Locate and identify every blood parasite.
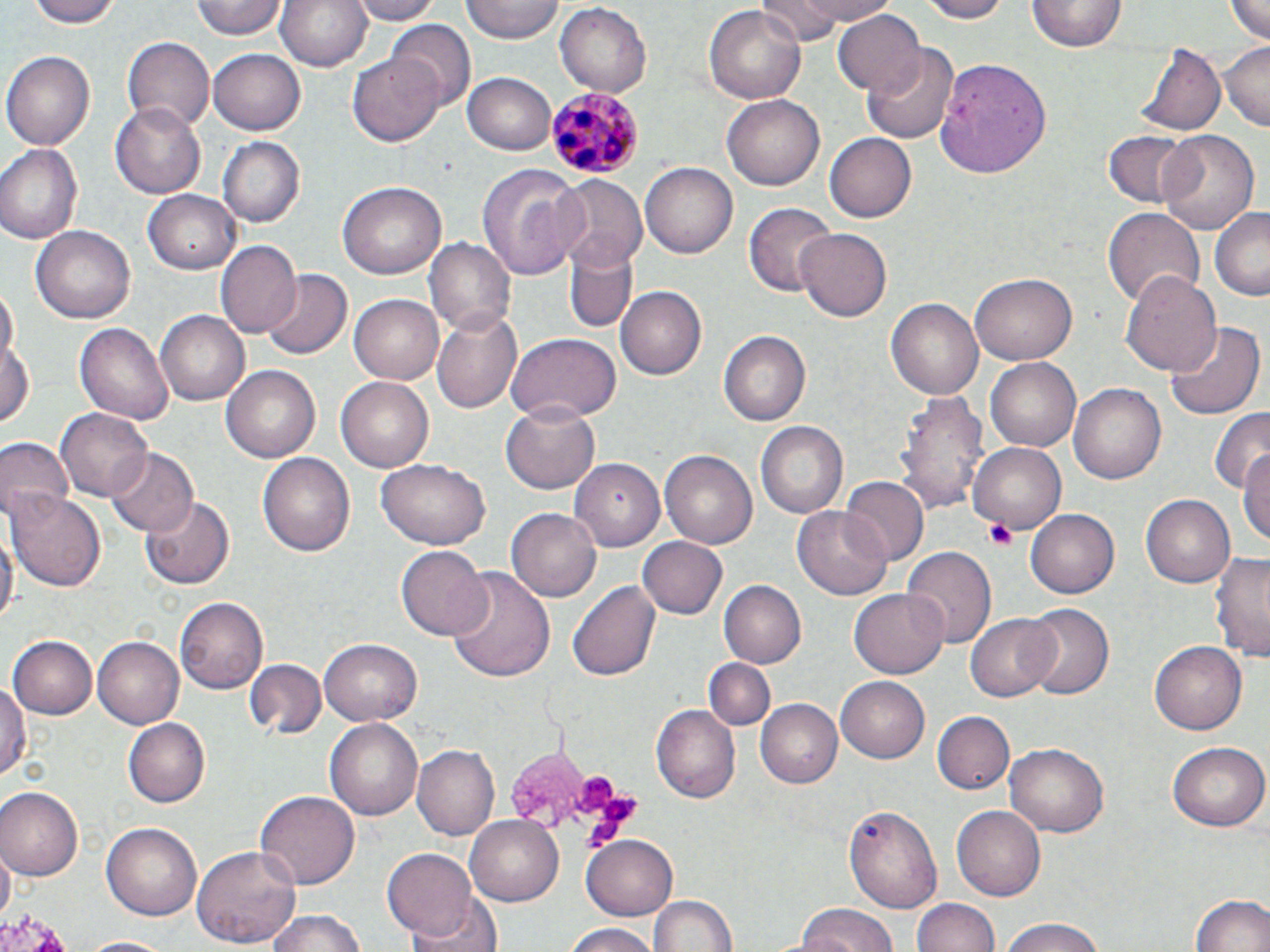
Approximate bounding boxes as [x1, y1, x2, y2] in pixels.
Plasmodium malariae-infected red blood cells: [545, 86, 644, 176].
No Plasmodium falciparum, Plasmodium ovale, Plasmodium vivax, Babesia divergens, or Trypanosoma brucei observed.

Platelet locations: [985, 520, 1016, 551], [572, 771, 614, 812], [586, 796, 642, 839]. Uninfected red blood cell locations: [27, 0, 123, 27], [194, 0, 287, 40], [276, 0, 373, 73], [349, 0, 440, 24], [461, 0, 564, 44], [762, 0, 840, 47], [786, 0, 896, 25], [915, 0, 1011, 23], [1224, 0, 1270, 44], [554, 1, 655, 97], [1027, 2, 1125, 53], [704, 3, 806, 106], [833, 9, 925, 98], [391, 23, 475, 109], [123, 35, 213, 131], [1218, 41, 1270, 129], [1138, 42, 1227, 139], [863, 44, 960, 146], [210, 48, 305, 135], [4, 52, 95, 149], [347, 54, 444, 147], [936, 57, 1051, 177], [464, 74, 555, 155], [721, 90, 825, 190], [113, 99, 210, 197], [1156, 130, 1260, 236], [1105, 131, 1192, 207], [825, 134, 916, 222], [217, 137, 304, 228], [1, 145, 83, 243], [641, 161, 738, 258], [477, 162, 588, 277], [551, 173, 649, 271], [338, 181, 446, 279], [144, 190, 242, 273], [742, 201, 835, 297], [1211, 206, 1270, 300], [1103, 207, 1206, 306], [32, 224, 136, 324], [795, 227, 894, 321], [424, 235, 515, 337], [217, 243, 302, 339], [566, 246, 635, 332], [261, 268, 351, 361], [1121, 271, 1223, 377], [972, 273, 1076, 364], [615, 283, 706, 378], [1, 289, 18, 367], [351, 294, 448, 385], [887, 298, 985, 401], [156, 309, 250, 405], [432, 310, 524, 413], [1166, 321, 1264, 423], [75, 323, 174, 424], [720, 330, 810, 426], [506, 333, 622, 424], [0, 341, 36, 428], [988, 357, 1084, 452], [222, 364, 322, 463], [336, 376, 434, 473], [1069, 383, 1167, 483], [899, 392, 989, 520], [501, 404, 600, 494], [57, 407, 152, 504], [1209, 408, 1270, 499], [755, 421, 847, 519], [1, 437, 72, 522], [969, 442, 1066, 534], [1237, 445, 1270, 546], [103, 446, 198, 536], [659, 450, 757, 549], [260, 453, 355, 558], [377, 459, 491, 548], [571, 459, 665, 550], [841, 477, 929, 567], [8, 488, 105, 587], [1141, 494, 1235, 587], [138, 495, 237, 589], [1025, 505, 1120, 596], [793, 508, 892, 598], [506, 509, 599, 600], [0, 526, 16, 633], [639, 535, 728, 619], [903, 545, 996, 648], [397, 546, 491, 640], [1211, 552, 1269, 663], [446, 567, 555, 685], [720, 579, 809, 669], [567, 580, 660, 684], [850, 588, 948, 679], [177, 597, 271, 692], [1017, 603, 1116, 701], [966, 614, 1059, 703], [9, 635, 97, 720], [91, 636, 182, 728], [320, 636, 422, 723], [1151, 640, 1247, 734], [703, 658, 776, 731], [244, 659, 325, 740], [0, 673, 29, 783], [835, 675, 930, 762], [756, 698, 843, 788], [651, 703, 742, 803], [933, 711, 1015, 794], [124, 718, 210, 807], [326, 718, 424, 821], [1167, 741, 1266, 830], [1006, 742, 1106, 837], [412, 744, 498, 840], [0, 787, 82, 879], [255, 788, 358, 887], [844, 804, 944, 912], [952, 804, 1046, 900], [466, 814, 565, 904], [100, 822, 202, 921], [579, 834, 678, 916], [193, 843, 302, 949], [385, 847, 479, 940], [0, 852, 13, 922], [1188, 891, 1270, 952], [644, 892, 740, 952], [404, 895, 503, 952], [913, 898, 1002, 952], [792, 905, 900, 952], [262, 908, 371, 952], [998, 916, 1109, 952], [560, 924, 665, 952], [76, 935, 177, 952]. Slide-level diagnosis: Plasmodium malariae. Image is 1270×952 pixels. Thin blood film. One field of a larger specimen. Optical microscopy. May-Grünwald-Giemsa stain. 1000x magnification.